Assess this cell for malaria.
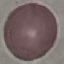
It is uninfected.

preparation = thin blood smear
image type = cell patch, automatically extracted from a larger field of view and resized to 64 × 64 pixels
stain = Giemsa
capture = smartphone camera at the microscope eyepiece